Evaluate for Plasmodium parasites.
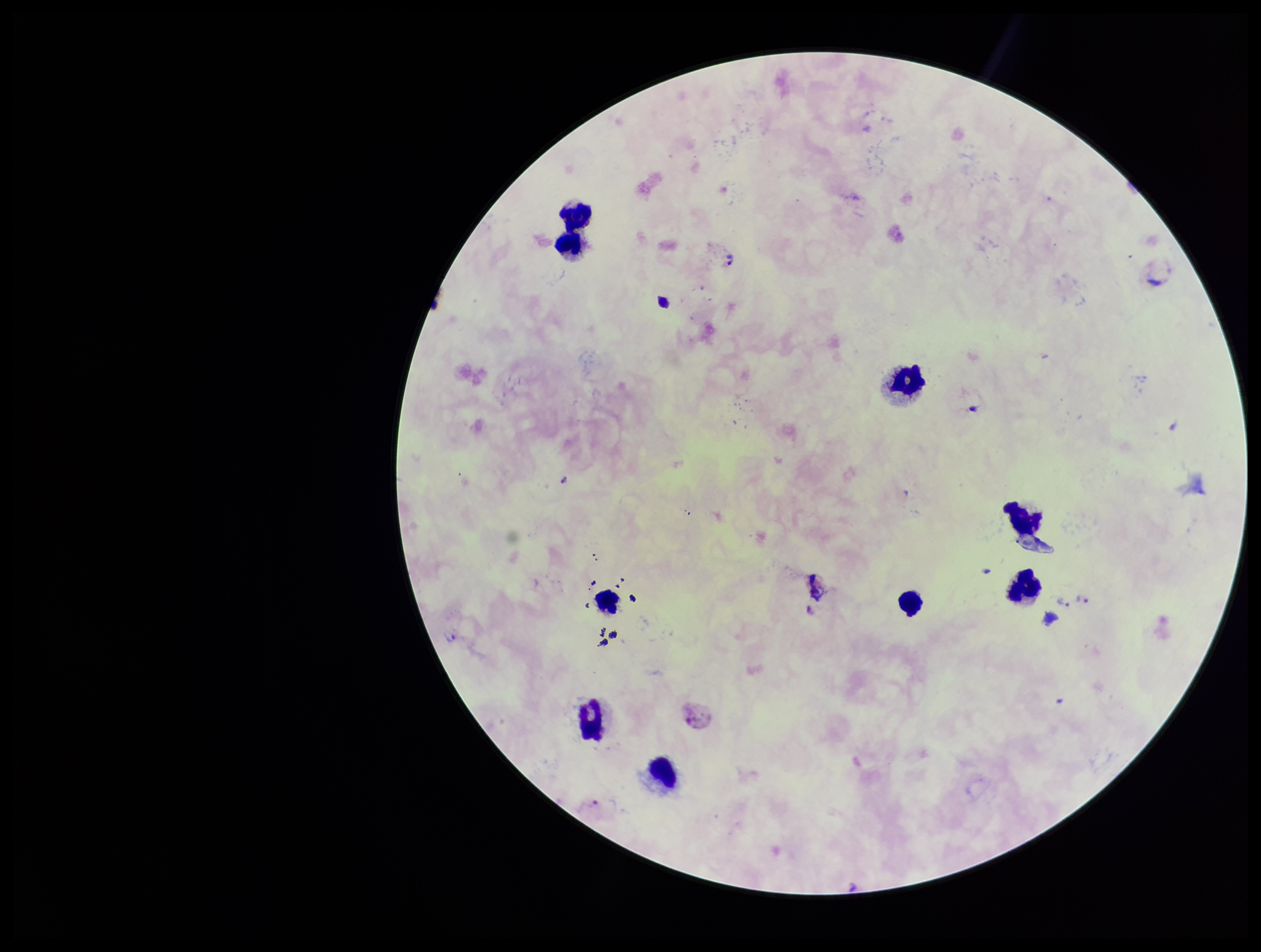

Seen.

Summary:
  - Stain: Giemsa
  - Parasite count: 8
  - Species reported for this patient: Plasmodium vivax
  - Field of view: one from this slide
  - Preparation: thick smear
  - Image size: 1261×952 pixels
  - Patient malaria status: positive
  - Capture: smartphone photograph through the microscope eyepiece
  - Leukocyte count: 9